Locate every blood parasite and identify its species.
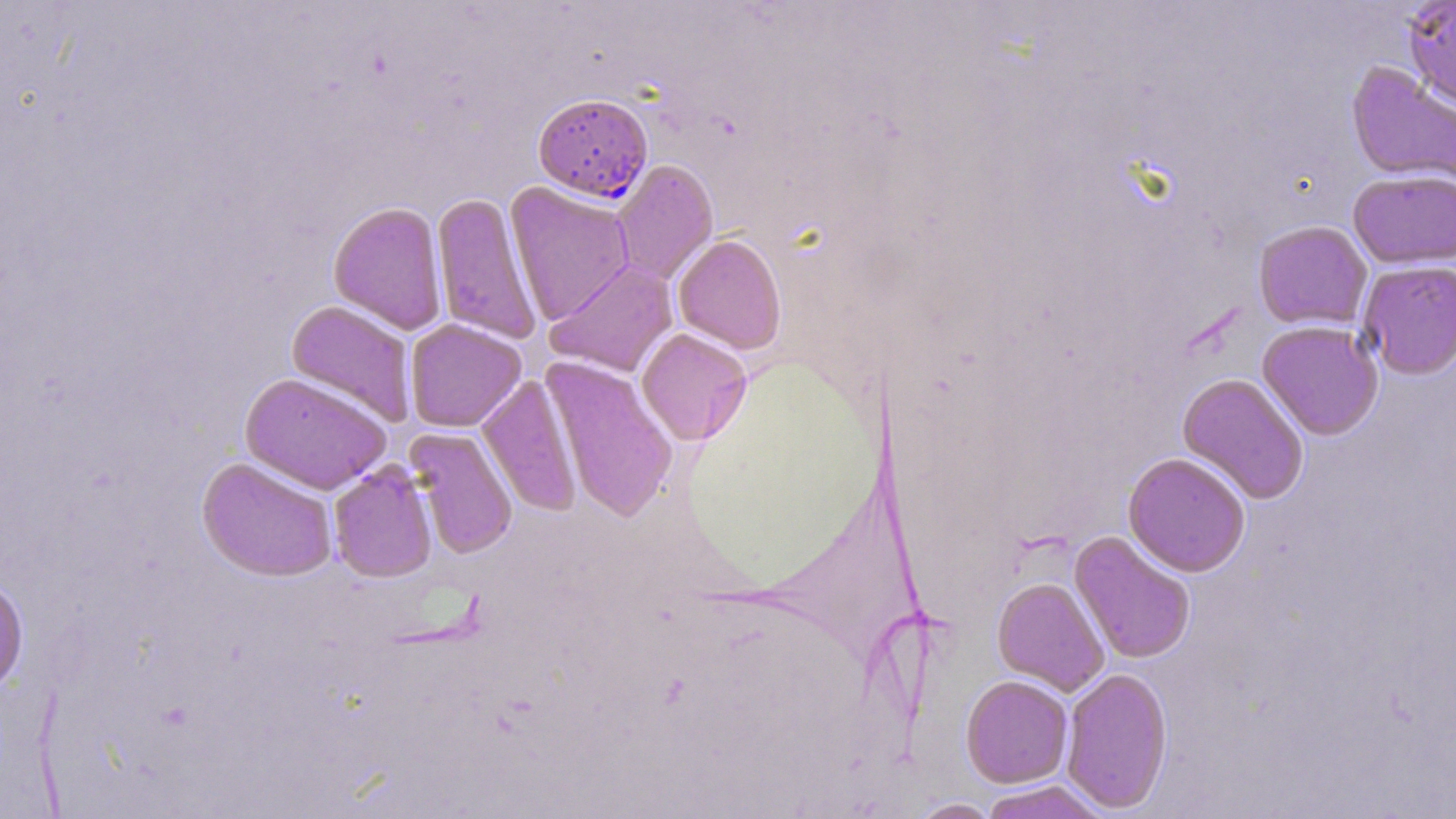

Approximate bounding boxes as (x1,y1)-(x2,y2) corner pairs in pixels.
Plasmodium falciparum-infected red blood cells: (533,93)-(653,202).
No Plasmodium ovale, Plasmodium malariae, Plasmodium vivax, Babesia divergens, or Trypanosoma brucei observed.

Uninfected red blood cell locations: (1401,0)-(1456,112), (1346,62)-(1456,188), (611,159)-(719,286), (1348,169)-(1456,269), (504,181)-(635,326), (430,192)-(542,345), (329,200)-(448,335), (1253,220)-(1373,330), (673,234)-(787,354), (544,260)-(678,378), (1358,261)-(1456,379), (286,300)-(417,428), (405,319)-(526,432), (1257,321)-(1384,441), (636,327)-(753,445), (542,356)-(678,522), (238,372)-(393,495), (1177,373)-(1310,504), (477,376)-(582,515), (406,426)-(518,559), (1123,452)-(1251,577), (197,456)-(339,582), (328,459)-(437,583), (1070,531)-(1196,664), (0,574)-(28,697), (992,577)-(1109,696), (1061,666)-(1173,813), (960,675)-(1073,788), (978,780)-(1110,819), (908,798)-(1001,819). Slide-level diagnosis: Plasmodium falciparum. Light microscopy. Thin blood film. Single field of view. Captured at 1000x magnification. Image is 1456×819 pixels. May-Grünwald-Giemsa stain.